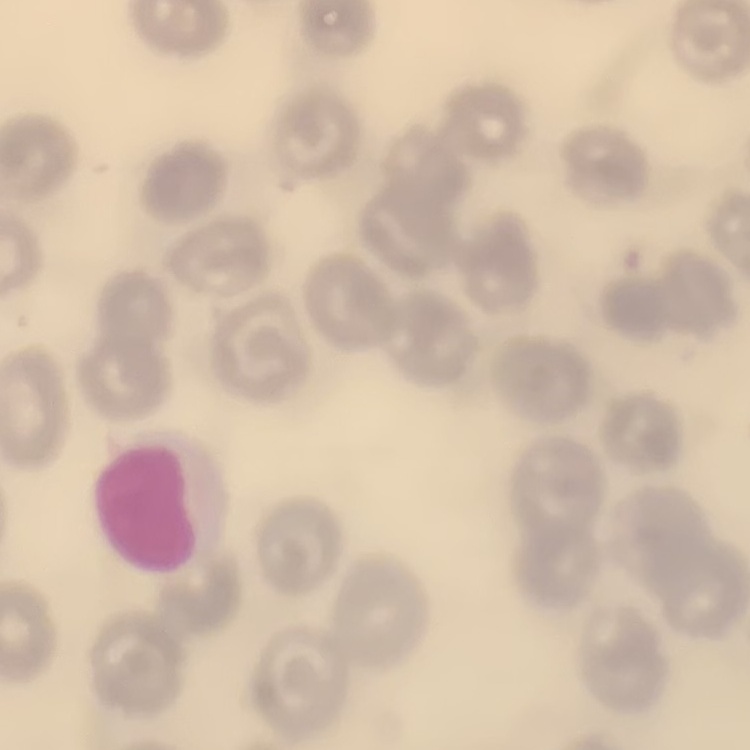
Summary:
  - Red blood cell morphology: no rouleaux formation
  - Preparation: thin blood smear
  - Image type: square crop of a larger photomicrograph
  - Stain: Field's or Giemsa